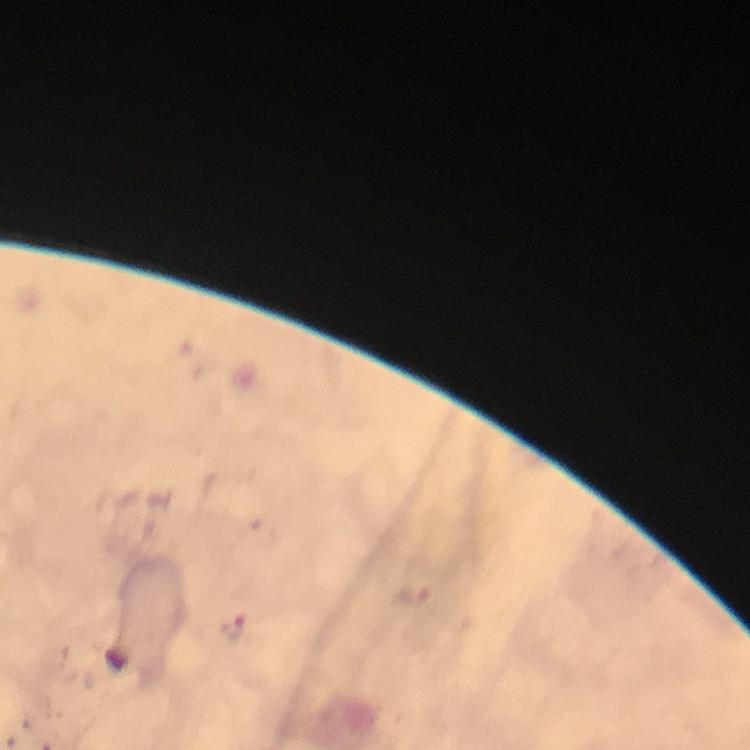
malaria parasite locations = approximate centers as (x, y) in pixels: (234, 628)
image size = 750×750 pixels
capture = smartphone photograph through a microscope
preparation = thick blood film
context = from a malaria diagnostic workup
immersion oil = applied
stain = Giemsa
cropped from = one field of view
magnification = 100x